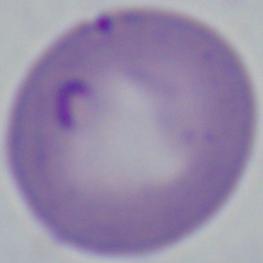
modality = micrograph
identification = Babesia
magnification = 1000x